Name the blood parasite species.
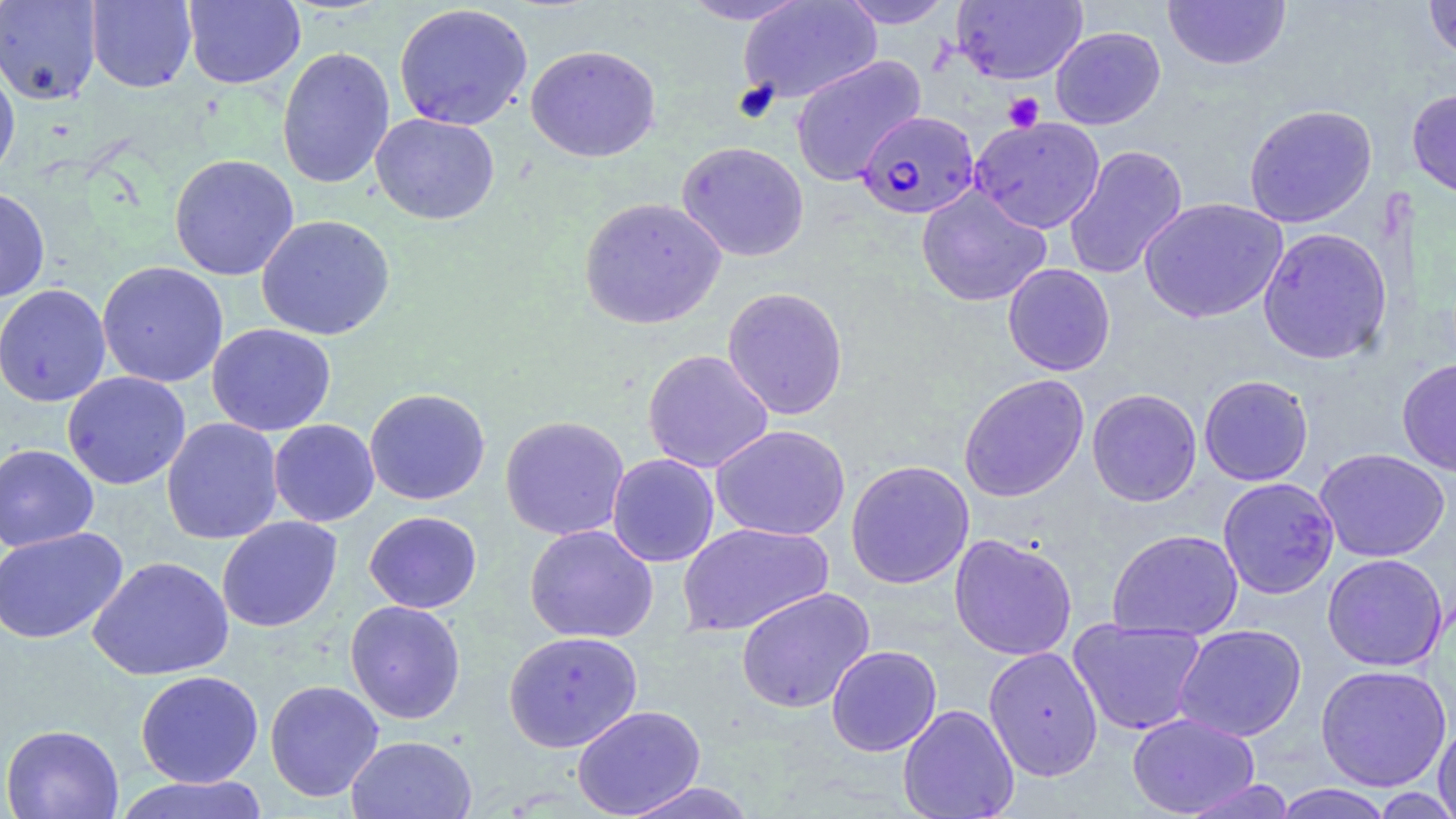

Plasmodium falciparum.

platelet locations = approximate bounding boxes as named x1/y1/x2/y2 corners in pixels: (x1=1003, y1=92, x2=1045, y2=132)
uninfected red blood cell locations = approximate bounding boxes as named x1/y1/x2/y2 corners in pixels: (x1=0, y1=0, x2=101, y2=105), (x1=85, y1=0, x2=197, y2=93), (x1=183, y1=0, x2=305, y2=89), (x1=677, y1=0, x2=813, y2=25), (x1=737, y1=0, x2=881, y2=104), (x1=838, y1=0, x2=956, y2=28), (x1=951, y1=0, x2=1087, y2=85), (x1=1162, y1=0, x2=1291, y2=71), (x1=1423, y1=0, x2=1456, y2=63), (x1=393, y1=3, x2=533, y2=131), (x1=1050, y1=27, x2=1165, y2=129), (x1=525, y1=44, x2=661, y2=163), (x1=277, y1=46, x2=396, y2=190), (x1=790, y1=55, x2=926, y2=186), (x1=0, y1=61, x2=21, y2=183), (x1=1407, y1=88, x2=1456, y2=199), (x1=1243, y1=104, x2=1378, y2=228), (x1=370, y1=112, x2=500, y2=225), (x1=970, y1=116, x2=1106, y2=234), (x1=676, y1=141, x2=809, y2=262), (x1=1064, y1=144, x2=1188, y2=280), (x1=169, y1=153, x2=299, y2=281), (x1=916, y1=186, x2=1052, y2=307), (x1=0, y1=187, x2=50, y2=302), (x1=579, y1=197, x2=726, y2=330), (x1=1139, y1=197, x2=1288, y2=323), (x1=255, y1=214, x2=396, y2=341), (x1=1257, y1=227, x2=1393, y2=364), (x1=97, y1=261, x2=229, y2=388), (x1=1002, y1=263, x2=1115, y2=375), (x1=0, y1=284, x2=112, y2=407), (x1=722, y1=286, x2=849, y2=420), (x1=207, y1=323, x2=336, y2=436), (x1=642, y1=349, x2=774, y2=473), (x1=1396, y1=357, x2=1456, y2=477), (x1=62, y1=371, x2=191, y2=490), (x1=958, y1=373, x2=1090, y2=503), (x1=1198, y1=374, x2=1314, y2=486), (x1=364, y1=388, x2=491, y2=505), (x1=1086, y1=388, x2=1202, y2=507), (x1=499, y1=415, x2=630, y2=541), (x1=161, y1=417, x2=283, y2=545), (x1=268, y1=419, x2=380, y2=527), (x1=711, y1=424, x2=851, y2=541), (x1=0, y1=444, x2=99, y2=552), (x1=1314, y1=447, x2=1450, y2=562), (x1=606, y1=453, x2=720, y2=567), (x1=845, y1=460, x2=975, y2=589), (x1=1217, y1=477, x2=1340, y2=599), (x1=363, y1=511, x2=482, y2=613), (x1=216, y1=516, x2=343, y2=633), (x1=676, y1=523, x2=834, y2=636), (x1=524, y1=524, x2=658, y2=643), (x1=0, y1=527, x2=128, y2=645), (x1=1107, y1=528, x2=1243, y2=641), (x1=949, y1=533, x2=1078, y2=661), (x1=1321, y1=553, x2=1449, y2=671), (x1=88, y1=556, x2=233, y2=681), (x1=735, y1=586, x2=875, y2=713), (x1=344, y1=600, x2=467, y2=724), (x1=1068, y1=618, x2=1207, y2=736), (x1=1173, y1=624, x2=1307, y2=742), (x1=503, y1=630, x2=643, y2=752), (x1=825, y1=644, x2=943, y2=756), (x1=983, y1=646, x2=1104, y2=781), (x1=1314, y1=664, x2=1452, y2=791), (x1=135, y1=669, x2=264, y2=788), (x1=264, y1=679, x2=384, y2=802), (x1=898, y1=703, x2=1019, y2=819), (x1=572, y1=704, x2=706, y2=818), (x1=1127, y1=712, x2=1260, y2=817), (x1=1433, y1=720, x2=1456, y2=819), (x1=1, y1=723, x2=124, y2=819), (x1=346, y1=735, x2=478, y2=819), (x1=112, y1=774, x2=271, y2=819), (x1=1180, y1=779, x2=1297, y2=819), (x1=618, y1=781, x2=758, y2=819), (x1=1268, y1=785, x2=1396, y2=819)
modality = light microscopy
magnification = 1000x
image size = 1456×819 pixels
preparation = thin blood film
stain = May-Grünwald-Giemsa
field of view = single
Plasmodium falciparum-infected red blood cell locations = approximate bounding boxes as named x1/y1/x2/y2 corners in pixels: (x1=860, y1=106, x2=984, y2=215)